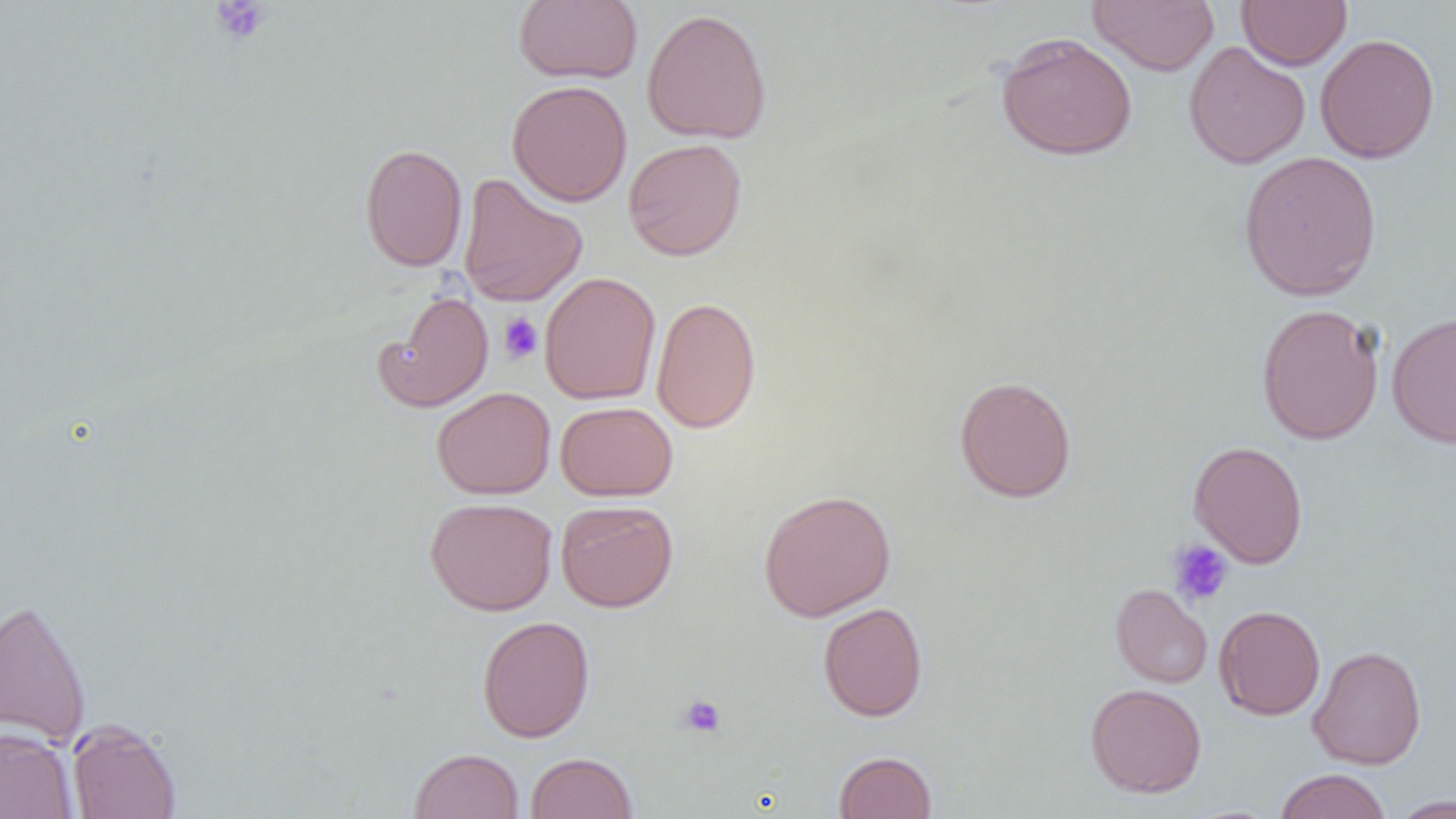

slide_level_diagnosis: negative for blood parasites
modality: optical microscopy
preparation: thin blood smear
uninfected_red_blood_cell_locations: 'approximate bounding boxes as named x1/y1/x2/y2 corners in pixels: (x1=512, y1=0, x2=643, y2=84), (x1=1087, y1=0, x2=1219, y2=76), (x1=1237, y1=0, x2=1352, y2=70), (x1=641, y1=8, x2=772, y2=144), (x1=994, y1=31, x2=1138, y2=161), (x1=1315, y1=33, x2=1440, y2=164), (x1=1183, y1=41, x2=1310, y2=169), (x1=507, y1=80, x2=632, y2=207), (x1=623, y1=138, x2=747, y2=261), (x1=359, y1=142, x2=468, y2=272), (x1=1238, y1=150, x2=1382, y2=301), (x1=457, y1=173, x2=588, y2=307), (x1=539, y1=271, x2=661, y2=404), (x1=373, y1=290, x2=494, y2=413), (x1=650, y1=296, x2=761, y2=434), (x1=1255, y1=303, x2=1385, y2=445), (x1=1387, y1=309, x2=1456, y2=448), (x1=954, y1=375, x2=1077, y2=503), (x1=431, y1=386, x2=556, y2=499), (x1=555, y1=401, x2=677, y2=501), (x1=1188, y1=440, x2=1309, y2=568), (x1=758, y1=489, x2=896, y2=621), (x1=425, y1=496, x2=558, y2=615), (x1=556, y1=499, x2=678, y2=612), (x1=1111, y1=583, x2=1213, y2=688), (x1=0, y1=597, x2=92, y2=747), (x1=818, y1=602, x2=929, y2=722), (x1=1214, y1=605, x2=1326, y2=720), (x1=477, y1=615, x2=595, y2=743), (x1=1308, y1=645, x2=1427, y2=769), (x1=1085, y1=683, x2=1206, y2=798), (x1=66, y1=719, x2=182, y2=819), (x1=0, y1=727, x2=78, y2=819), (x1=410, y1=748, x2=524, y2=819), (x1=834, y1=750, x2=937, y2=818), (x1=525, y1=751, x2=637, y2=818), (x1=1274, y1=769, x2=1392, y2=819), (x1=1388, y1=795, x2=1455, y2=818)'
magnification: 1000x
image_size: 1456×819 pixels
field_of_view: one of a larger specimen
platelet_locations: 'approximate bounding boxes as named x1/y1/x2/y2 corners in pixels: (x1=210, y1=1, x2=272, y2=45), (x1=498, y1=312, x2=543, y2=364), (x1=1167, y1=540, x2=1233, y2=606), (x1=677, y1=694, x2=727, y2=739)'